Identify the blood parasite species.
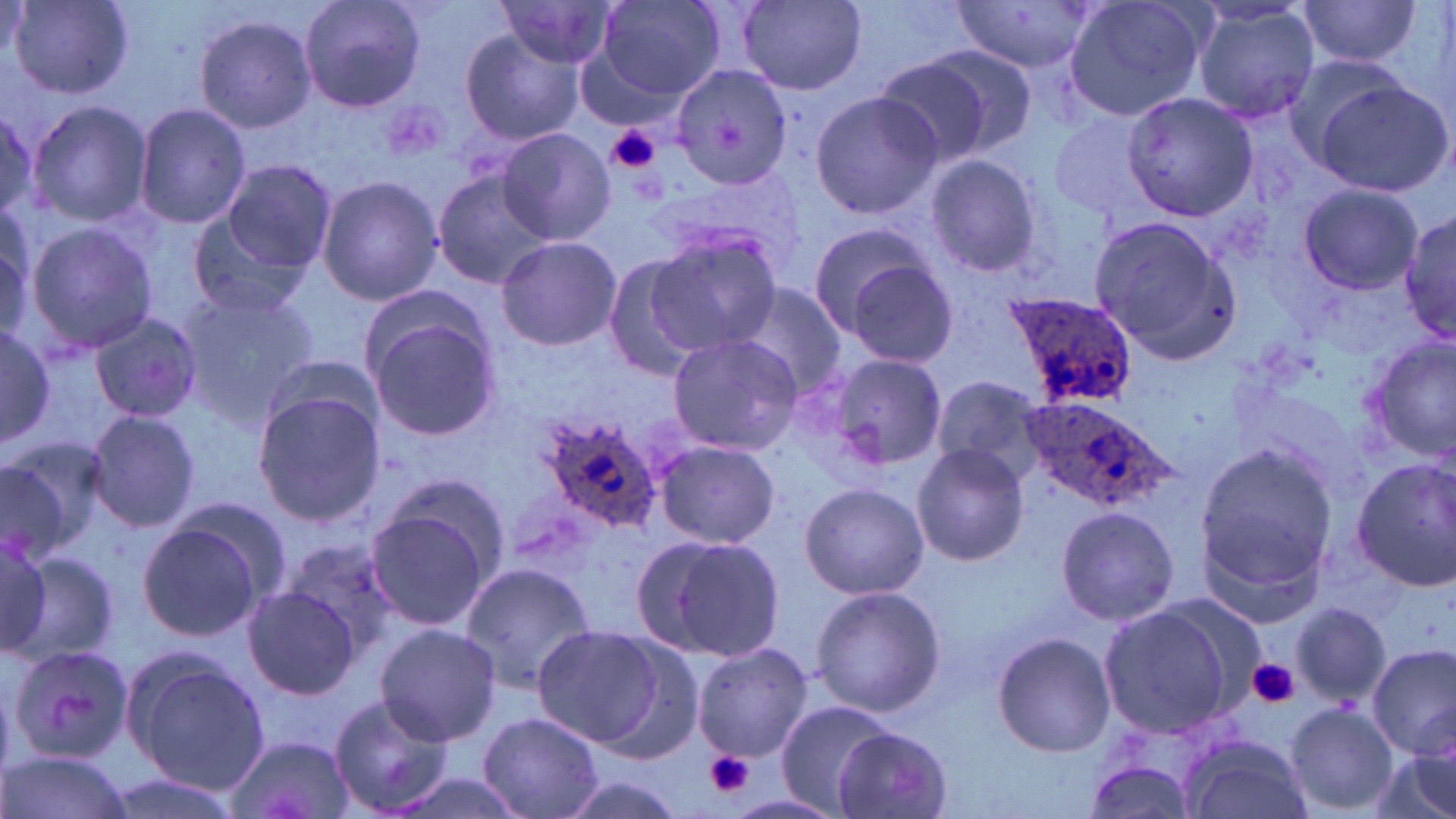

Plasmodium ovale.

Summary:
  - Coordinate format: approximate bounding boxes as [x1, y1, x2, y2] in pixels
  - Uninfected red blood cell locations: [299, 0, 426, 113], [589, 0, 727, 106], [1058, 0, 1212, 122], [6, 1, 134, 98], [496, 1, 622, 71], [736, 1, 867, 94], [1296, 1, 1427, 67], [947, 2, 1102, 73], [1191, 3, 1321, 126], [194, 12, 318, 132], [457, 28, 586, 146], [913, 42, 1039, 158], [1281, 53, 1423, 172], [872, 57, 994, 168], [674, 64, 791, 190], [1312, 81, 1453, 198], [807, 89, 943, 219], [1121, 91, 1261, 222], [28, 101, 152, 228], [134, 102, 252, 230], [0, 103, 37, 224], [1048, 108, 1163, 221], [497, 127, 615, 245], [923, 154, 1046, 279], [219, 158, 336, 274], [432, 171, 557, 289], [316, 174, 443, 306], [1297, 183, 1423, 295], [1400, 209, 1456, 344], [186, 215, 312, 319], [1085, 215, 1241, 360], [804, 219, 943, 338], [23, 221, 158, 356], [644, 227, 782, 357], [495, 235, 622, 350], [836, 250, 960, 368], [601, 255, 708, 382], [731, 284, 847, 397], [175, 286, 320, 421], [363, 303, 505, 444], [89, 313, 204, 424], [0, 319, 56, 454], [665, 333, 805, 456], [1365, 337, 1456, 461], [832, 355, 945, 470], [932, 373, 1048, 481], [251, 388, 385, 528], [85, 409, 201, 532], [656, 439, 779, 549], [0, 440, 104, 560], [911, 443, 1030, 566], [1195, 443, 1340, 586], [1351, 458, 1456, 593], [378, 475, 511, 587], [798, 482, 928, 600], [363, 500, 495, 636], [1057, 502, 1179, 628], [136, 519, 269, 642], [646, 533, 788, 661], [0, 539, 52, 658], [282, 540, 402, 657], [12, 547, 118, 669], [460, 559, 596, 690], [810, 584, 947, 717], [244, 585, 361, 700], [1289, 600, 1391, 709], [1096, 602, 1242, 739], [375, 623, 501, 747], [530, 624, 672, 751], [991, 631, 1116, 757], [586, 635, 707, 763], [693, 642, 812, 761], [1369, 644, 1454, 760], [5, 645, 131, 768], [121, 650, 268, 794], [327, 693, 454, 817], [773, 700, 894, 816], [1285, 703, 1397, 814], [478, 711, 602, 818], [834, 728, 953, 817], [224, 733, 355, 819], [1180, 733, 1312, 819], [1375, 735, 1455, 819], [2, 750, 132, 819], [1082, 756, 1198, 819], [377, 770, 533, 819], [554, 771, 690, 819], [94, 772, 246, 819]
  - Platelet locations: [603, 124, 662, 175], [1246, 658, 1300, 708], [703, 752, 757, 800]
  - Plasmodium ovale-infected red blood cell locations: [998, 290, 1140, 413], [1017, 396, 1175, 512], [534, 414, 667, 534]
  - Stain: May-Grünwald-Giemsa
  - Field of view: one of a larger specimen
  - Image size: 1456×819 pixels
  - Preparation: thin blood smear
  - Magnification: 1000x
  - Modality: optical microscopy